Comment on the morphology of the erythrocytes.
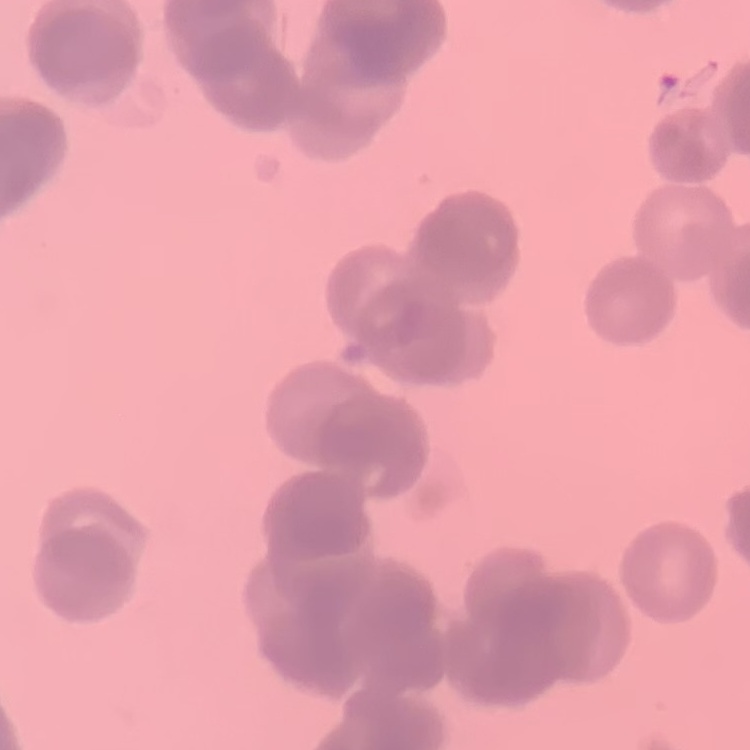
Rouleaux formation.

Thin peripheral smear. Stained with either Field's or Giemsa. One tile cut from a larger photomicrograph.